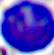

magnification = 400x
identification = leukocyte
modality = micrograph